State which cell type is depicted.
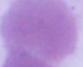

An erythrocyte.

Summary:
  - Magnification: 1000x
  - Modality: photomicrograph